State the blood parasite species.
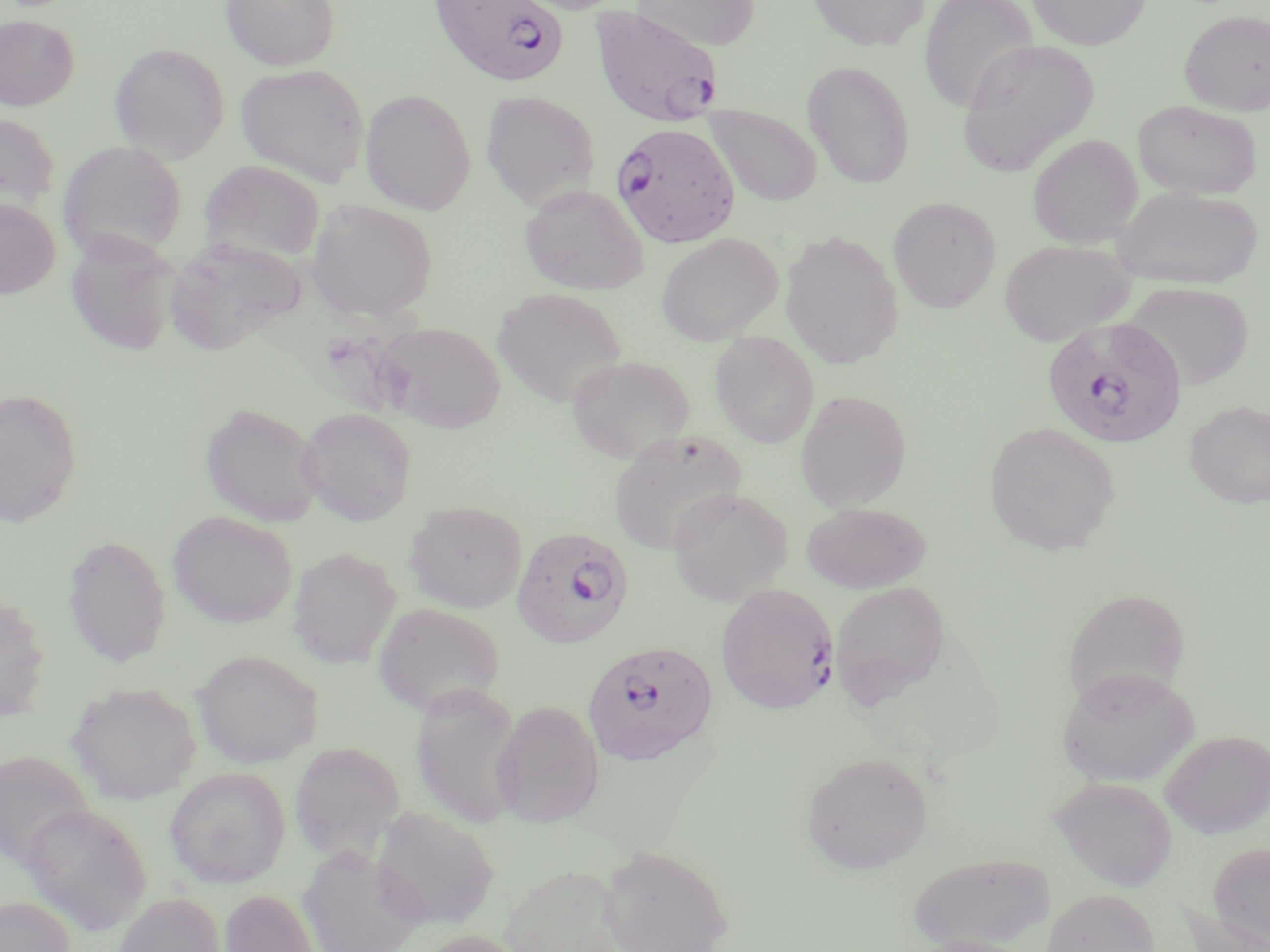

Plasmodium falciparum.

{
  "image_size": "1270×952 pixels",
  "plasmodium_falciparum_infected_red_blood_cell_locations": "approximate bounding boxes as named x1/y1/x2/y2 corners in pixels: (x1=434, y1=0, x2=567, y2=88), (x1=589, y1=5, x2=725, y2=129), (x1=611, y1=121, x2=739, y2=248), (x1=1041, y1=316, x2=1187, y2=449), (x1=511, y1=526, x2=633, y2=647), (x1=716, y1=583, x2=838, y2=714), (x1=582, y1=640, x2=719, y2=767)",
  "modality": "light microscopy",
  "uninfected_red_blood_cell_locations": "approximate bounding boxes as named x1/y1/x2/y2 corners in pixels: (x1=221, y1=0, x2=340, y2=70), (x1=631, y1=0, x2=760, y2=50), (x1=807, y1=0, x2=929, y2=50), (x1=919, y1=0, x2=1039, y2=113), (x1=1027, y1=0, x2=1150, y2=50), (x1=1180, y1=10, x2=1270, y2=115), (x1=0, y1=14, x2=79, y2=112), (x1=957, y1=38, x2=1100, y2=176), (x1=109, y1=42, x2=229, y2=161), (x1=802, y1=60, x2=916, y2=188), (x1=236, y1=64, x2=368, y2=186), (x1=360, y1=89, x2=476, y2=215), (x1=481, y1=91, x2=600, y2=210), (x1=1132, y1=100, x2=1263, y2=199), (x1=704, y1=104, x2=823, y2=207), (x1=0, y1=113, x2=60, y2=218), (x1=1027, y1=133, x2=1143, y2=248), (x1=58, y1=140, x2=187, y2=262), (x1=200, y1=159, x2=326, y2=264), (x1=519, y1=184, x2=649, y2=295), (x1=1112, y1=185, x2=1264, y2=290), (x1=888, y1=197, x2=1001, y2=312), (x1=0, y1=198, x2=60, y2=298), (x1=306, y1=198, x2=438, y2=322), (x1=780, y1=231, x2=903, y2=369), (x1=66, y1=233, x2=179, y2=355), (x1=655, y1=233, x2=783, y2=345), (x1=164, y1=238, x2=303, y2=356), (x1=999, y1=239, x2=1134, y2=346), (x1=1125, y1=281, x2=1254, y2=391), (x1=491, y1=287, x2=628, y2=408), (x1=373, y1=322, x2=505, y2=432), (x1=711, y1=332, x2=819, y2=448), (x1=567, y1=355, x2=695, y2=464), (x1=0, y1=387, x2=83, y2=526), (x1=795, y1=389, x2=912, y2=511), (x1=1184, y1=401, x2=1270, y2=509), (x1=200, y1=402, x2=324, y2=527), (x1=298, y1=407, x2=417, y2=526), (x1=983, y1=421, x2=1120, y2=555), (x1=609, y1=429, x2=746, y2=555), (x1=668, y1=488, x2=793, y2=605), (x1=404, y1=501, x2=527, y2=613), (x1=801, y1=502, x2=931, y2=593), (x1=168, y1=511, x2=297, y2=628), (x1=63, y1=535, x2=171, y2=666), (x1=288, y1=546, x2=400, y2=667), (x1=830, y1=580, x2=951, y2=705), (x1=1062, y1=587, x2=1192, y2=708), (x1=0, y1=595, x2=50, y2=720), (x1=372, y1=602, x2=506, y2=717), (x1=192, y1=649, x2=322, y2=767), (x1=1056, y1=666, x2=1198, y2=786), (x1=411, y1=682, x2=524, y2=829), (x1=67, y1=683, x2=201, y2=805), (x1=492, y1=700, x2=604, y2=827), (x1=1160, y1=730, x2=1270, y2=838), (x1=289, y1=741, x2=405, y2=861), (x1=0, y1=750, x2=94, y2=871), (x1=802, y1=752, x2=932, y2=874), (x1=164, y1=766, x2=291, y2=889), (x1=1051, y1=776, x2=1178, y2=891), (x1=22, y1=803, x2=152, y2=935), (x1=370, y1=806, x2=500, y2=930), (x1=1207, y1=842, x2=1270, y2=949), (x1=297, y1=844, x2=426, y2=952), (x1=599, y1=846, x2=733, y2=952), (x1=908, y1=851, x2=1055, y2=950), (x1=498, y1=864, x2=628, y2=952), (x1=1042, y1=888, x2=1160, y2=952), (x1=220, y1=889, x2=319, y2=952), (x1=111, y1=892, x2=225, y2=952), (x1=0, y1=896, x2=75, y2=952), (x1=1178, y1=898, x2=1270, y2=952), (x1=413, y1=930, x2=529, y2=952), (x1=902, y1=937, x2=1045, y2=952)",
  "field_of_view": "single",
  "stain": "May-Grünwald-Giemsa",
  "magnification": "1000x",
  "preparation": "thin blood film"
}